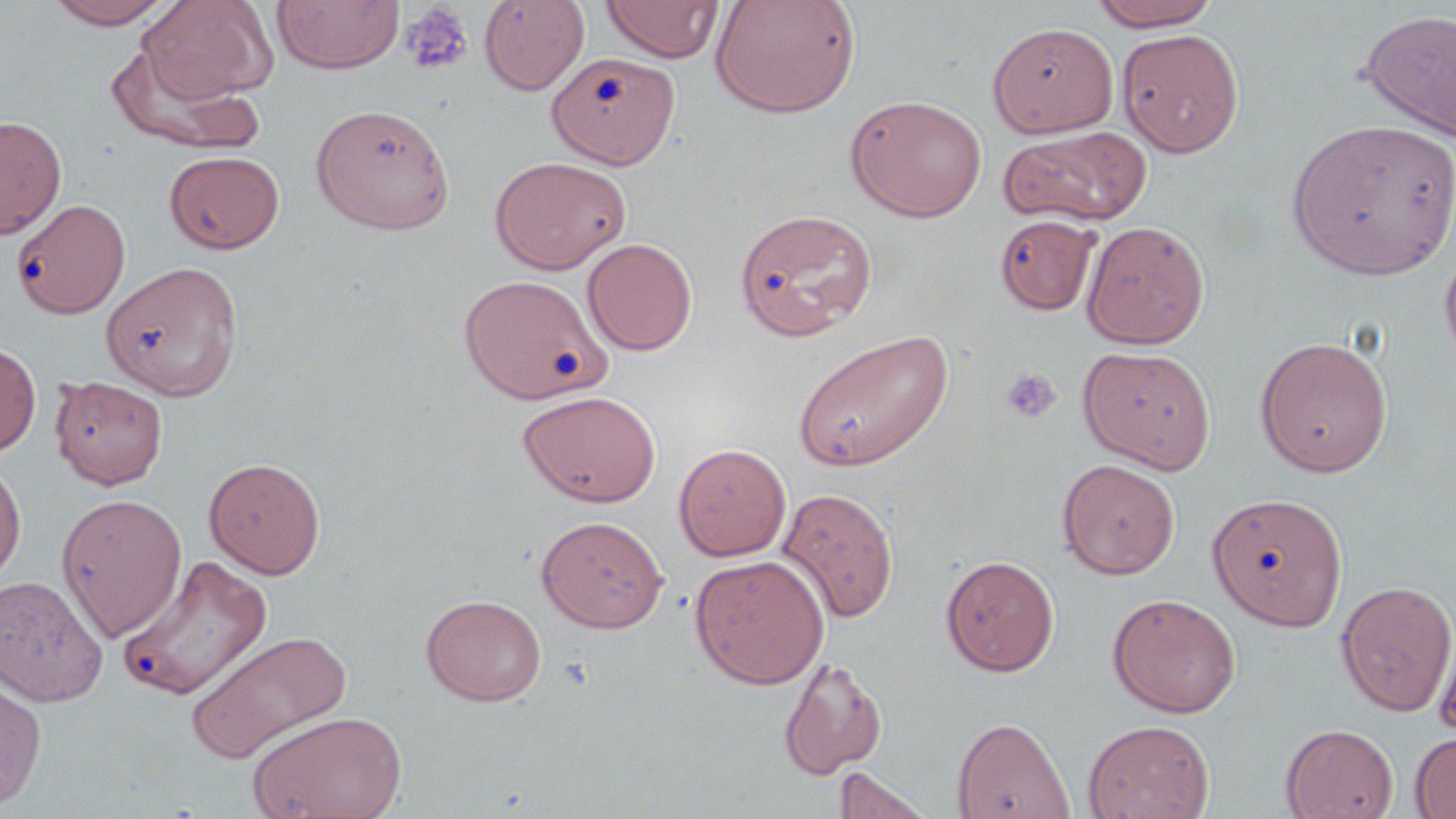

Summary:
  - Coordinate format: approximate bounding boxes as [x1, y1, x2, y2] in pixels
  - Platelet locations: [399, 3, 475, 75], [1000, 367, 1060, 425]
  - Uninfected red blood cell locations: [44, 0, 178, 29], [139, 0, 278, 103], [272, 0, 404, 75], [601, 0, 724, 62], [710, 0, 861, 119], [479, 1, 589, 95], [1089, 1, 1223, 30], [1358, 8, 1456, 143], [987, 22, 1117, 137], [1118, 28, 1245, 158], [105, 41, 264, 155], [547, 51, 680, 169], [845, 94, 987, 222], [311, 103, 455, 234], [0, 115, 66, 239], [1287, 118, 1456, 280], [999, 126, 1150, 227], [164, 150, 284, 254], [489, 156, 630, 274], [11, 197, 130, 318], [734, 208, 878, 341], [995, 214, 1100, 315], [1081, 220, 1210, 349], [583, 238, 698, 355], [1439, 242, 1456, 371], [102, 261, 243, 400], [459, 274, 611, 404], [792, 329, 953, 472], [1255, 335, 1393, 477], [0, 338, 41, 457], [1078, 345, 1216, 473], [49, 375, 168, 489], [517, 390, 661, 507], [673, 443, 792, 562], [0, 455, 26, 587], [204, 458, 326, 579], [1057, 459, 1180, 579], [775, 487, 899, 623], [1207, 491, 1348, 629], [56, 493, 188, 642], [535, 515, 669, 633], [690, 554, 830, 689], [941, 554, 1059, 676], [119, 555, 273, 701], [0, 575, 108, 707], [1336, 581, 1456, 717], [1107, 593, 1241, 718], [421, 594, 547, 706], [1433, 620, 1456, 744], [185, 629, 352, 765], [778, 657, 886, 780], [0, 679, 46, 812], [247, 710, 407, 819], [952, 716, 1074, 819], [1082, 719, 1215, 819], [1281, 724, 1398, 818], [1410, 731, 1456, 818], [834, 766, 933, 819]
  - Slide-level diagnosis: no evidence of blood parasites
  - Stain: May-Grünwald-Giemsa
  - Preparation: thin blood film
  - Field of view: one of a larger specimen
  - Magnification: 1000x
  - Image size: 1456×819 pixels
  - Modality: optical microscopy